State which parasite is depicted.
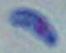
Toxoplasma gondii.

Summary:
  - Magnification: 1000x
  - Modality: photomicrograph